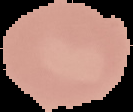
Image is 133×112 pixels. Result: no malaria parasites seen. Cell region segmented out of the field of view; the surrounding area is masked to black. From a thin blood smear.